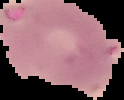
result = no malaria parasites seen
preparation = thin blood smear
image size = 124×100 pixels
image type = segmented cell region on a black background